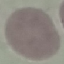
Result: no malaria parasites detected. Cell patch, automatically extracted from a larger field of view and resized to 64 × 64 pixels. Thin blood film. Photographed with a smartphone camera at the microscope eyepiece. Giemsa-stained preparation.